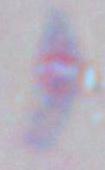

Summary:
  - Modality: photomicrograph
  - Magnification: 1000x
  - Identification: Toxoplasma gondii